Classify this cell by malaria status.
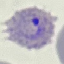
Parasitized.

capture: smartphone camera at the microscope eyepiece
stain: Giemsa
image_type: cell patch, automatically extracted from a larger field of view and resized to 64 × 64 pixels
preparation: thin smear